Outline platelets.
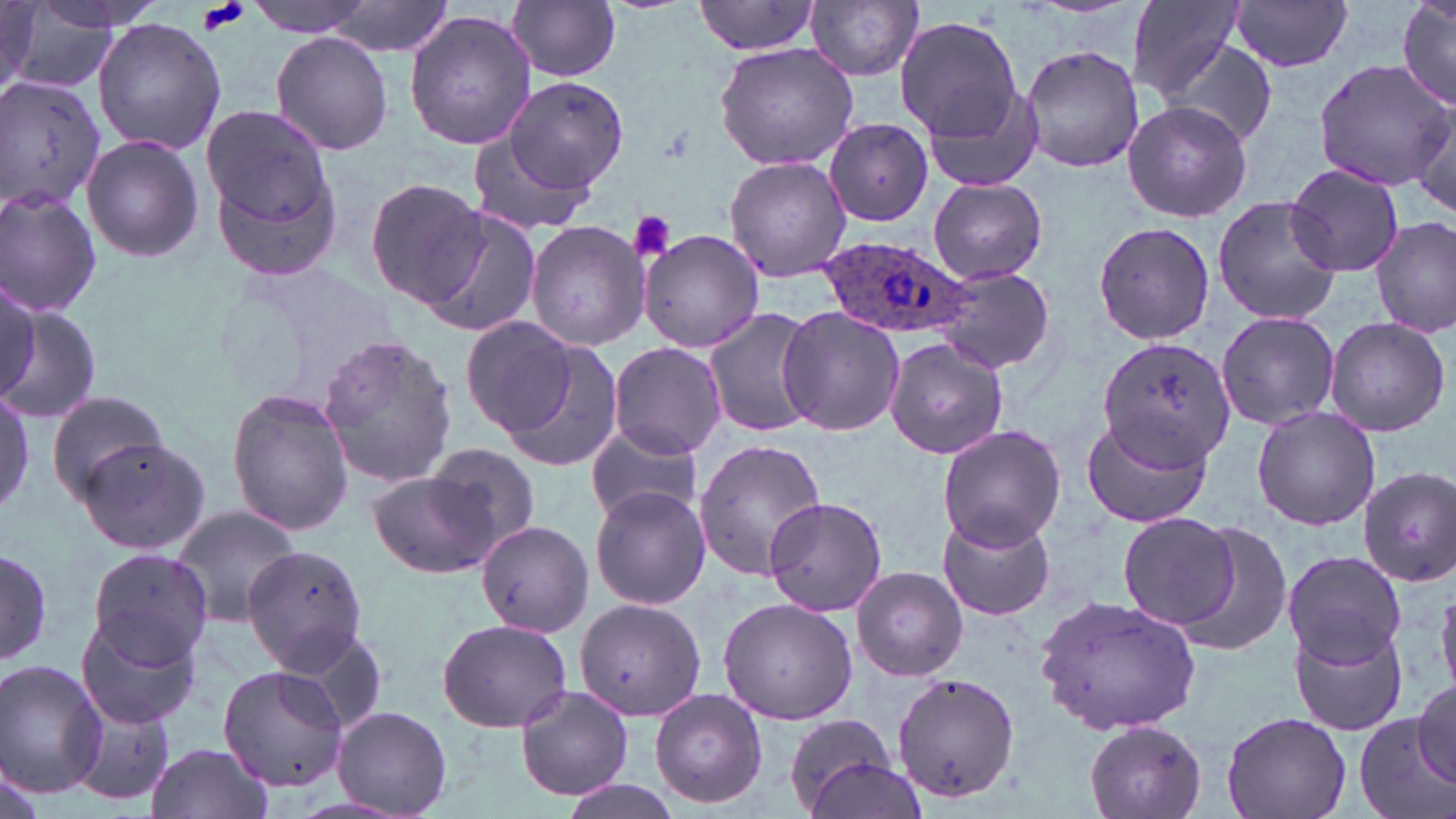

Approximate bounding boxes as (x1,y1)-(x2,y2) corner pairs in pixels.
Platelets: (198,0)-(252,34), (627,210)-(677,264).

Uninfected red blood cell locations: (246,0)-(380,35), (323,0)-(454,59), (1125,0)-(1246,99), (1395,0)-(1455,109), (0,1)-(40,91), (808,1)-(924,81), (1229,1)-(1354,72), (507,2)-(622,81), (689,2)-(824,60), (0,4)-(104,95), (406,12)-(537,152), (893,15)-(1023,139), (92,18)-(225,154), (270,30)-(394,156), (1160,37)-(1279,149), (713,43)-(860,171), (1018,45)-(1144,173), (1314,60)-(1451,188), (0,75)-(109,212), (502,75)-(631,191), (919,75)-(1051,194), (1405,98)-(1456,221), (1122,99)-(1252,223), (201,105)-(335,226), (824,117)-(934,228), (80,133)-(204,263), (467,134)-(593,237), (208,145)-(345,281), (723,155)-(851,282), (1283,162)-(1404,278), (364,177)-(487,308), (927,178)-(1048,283), (0,186)-(103,317), (1212,196)-(1343,324), (421,208)-(542,340), (1372,215)-(1455,337), (525,220)-(650,351), (1092,220)-(1214,346), (638,228)-(764,354), (934,266)-(1056,374), (0,277)-(40,409), (0,298)-(99,425), (701,308)-(820,439), (778,309)-(906,435), (1215,312)-(1340,431), (1325,317)-(1451,436), (463,319)-(585,441), (317,332)-(457,490), (1098,336)-(1236,469), (885,337)-(1008,459), (497,340)-(625,475), (609,342)-(728,459), (0,385)-(33,521), (228,388)-(354,534), (44,390)-(174,503), (1252,407)-(1382,531), (1082,412)-(1210,529), (937,425)-(1065,551), (586,430)-(702,521), (77,437)-(212,557), (691,439)-(826,581), (425,444)-(544,556), (1356,466)-(1456,585), (367,471)-(496,577), (589,485)-(710,608), (763,496)-(887,616), (169,503)-(302,628), (937,510)-(1054,620), (1117,511)-(1246,632), (474,519)-(591,637), (0,539)-(56,674), (244,542)-(375,677), (87,549)-(215,668), (1281,550)-(1409,667), (852,567)-(967,680), (1436,580)-(1456,697), (1034,593)-(1204,736), (575,595)-(705,722), (717,597)-(859,724), (77,611)-(204,730), (436,617)-(573,733), (1289,619)-(1410,738), (0,660)-(108,799), (219,664)-(347,793), (892,672)-(1023,802), (1414,679)-(1455,786), (516,685)-(635,800), (648,690)-(769,808), (69,694)-(176,804), (331,705)-(454,816), (1221,710)-(1352,819), (1356,717)-(1446,819), (784,718)-(914,819), (1083,719)-(1208,819), (146,741)-(275,819), (0,753)-(48,819), (559,777)-(691,819). Plasmodium ovale-infected red blood cell locations: (820,234)-(974,339). Slide-level diagnosis: Plasmodium ovale. One field of a larger specimen. Image is 1456×819 pixels. May-Grünwald-Giemsa stain. Thin blood smear. 1000x magnification. Optical microscopy.